Classify this cell by malaria status.
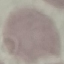

It is uninfected.

Giemsa-stained preparation. Automatically extracted cell patch, resized to 64 × 64 pixels. Photographed with a smartphone camera at the microscope eyepiece. Thin blood smear.